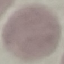

Summary:
  - Malaria status: uninfected
  - Stain: Giemsa
  - Capture: smartphone camera at the microscope eyepiece
  - Image type: cell patch, automatically extracted from a larger field of view and resized to 64 × 64 pixels
  - Preparation: thin blood smear